State which parasite is depicted.
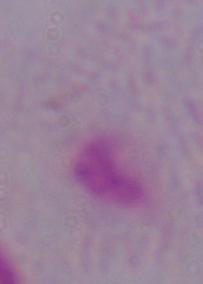

This is a trichomonad.

1000x magnification. Photomicrograph.